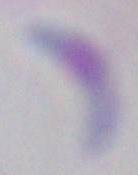

Toxoplasma gondii is seen. Micrograph. Captured at 1000x magnification.